Report the malaria status of this cell.
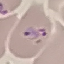

Parasitized.

Summary:
  - Capture: smartphone camera at the microscope eyepiece
  - Image type: cell patch, automatically extracted from a larger field of view and resized to 64 × 64 pixels
  - Stain: Giemsa
  - Preparation: thin blood film